Locate and identify every blood parasite.
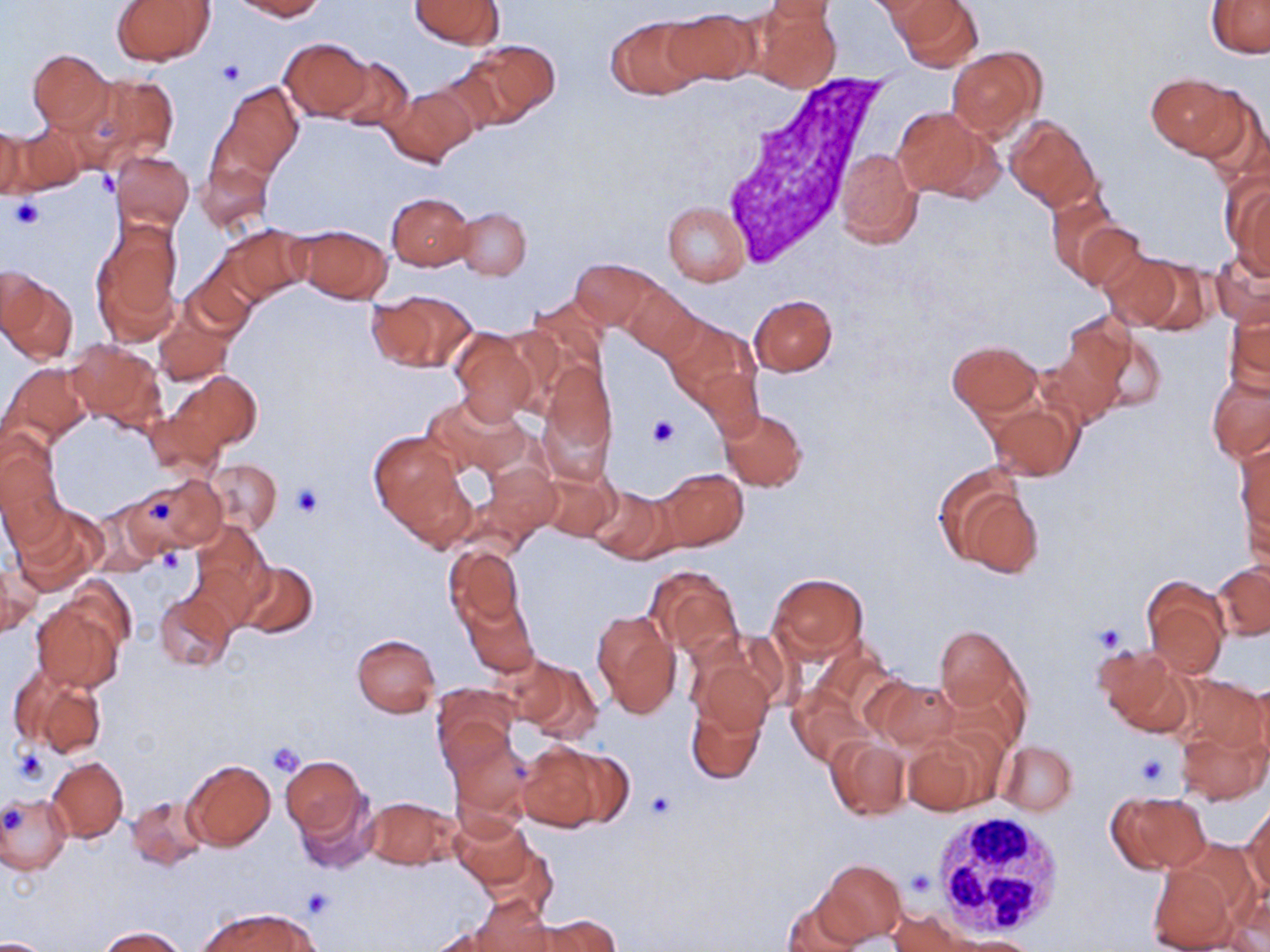

No blood parasites observed.

Approximate bounding boxes as (x1, y1, x2, y2) in pixels. White blood cell locations: (709, 71, 891, 265), (929, 811, 1064, 937). Platelet locations: (217, 61, 245, 87), (97, 170, 121, 197), (8, 198, 46, 230), (647, 416, 679, 447), (290, 485, 322, 519), (150, 499, 172, 519), (159, 550, 182, 573), (1092, 622, 1128, 653), (266, 742, 306, 778), (12, 746, 51, 784), (1134, 752, 1172, 790), (645, 791, 678, 823), (2, 808, 25, 835), (906, 870, 933, 897), (301, 887, 334, 918). Uninfected red blood cell locations: (234, 0, 325, 19), (410, 0, 502, 49), (764, 0, 840, 23), (896, 0, 980, 71), (113, 1, 216, 66), (1207, 2, 1270, 57), (663, 8, 758, 86), (753, 8, 840, 92), (607, 16, 705, 100), (281, 37, 373, 119), (460, 38, 560, 127), (27, 48, 113, 132), (947, 48, 1044, 139), (330, 55, 415, 132), (71, 73, 179, 169), (1147, 74, 1244, 157), (218, 82, 303, 176), (385, 86, 475, 165), (892, 106, 1000, 201), (1006, 116, 1099, 210), (0, 124, 26, 203), (6, 125, 85, 195), (834, 148, 922, 247), (111, 150, 194, 232), (196, 159, 272, 233), (1222, 175, 1270, 276), (387, 192, 475, 271), (1048, 194, 1124, 282), (661, 201, 749, 286), (457, 208, 530, 279), (89, 217, 182, 341), (1075, 222, 1149, 296), (222, 224, 309, 305), (291, 224, 395, 304), (1209, 248, 1270, 324), (1102, 251, 1193, 331), (570, 258, 657, 327), (180, 269, 256, 339), (1, 273, 77, 363), (624, 285, 700, 359), (367, 290, 475, 372), (526, 295, 608, 378), (750, 295, 836, 376), (1224, 300, 1269, 395), (155, 314, 233, 385), (664, 316, 759, 415), (448, 325, 540, 425), (1081, 325, 1167, 416), (1039, 335, 1125, 424), (65, 337, 166, 430), (948, 341, 1039, 418), (540, 362, 616, 467), (2, 363, 90, 447), (170, 373, 262, 457), (1207, 373, 1270, 463), (423, 394, 531, 481), (986, 401, 1081, 481), (719, 409, 807, 491), (144, 410, 224, 479), (0, 433, 65, 540), (369, 433, 463, 531), (1235, 440, 1270, 539), (207, 458, 282, 533), (484, 463, 562, 535), (935, 465, 1044, 578), (656, 469, 747, 550), (538, 471, 619, 542), (136, 472, 224, 552), (587, 486, 672, 563), (86, 502, 166, 576), (9, 505, 103, 595), (189, 520, 272, 622), (443, 545, 527, 633), (2, 558, 37, 640), (235, 560, 318, 639), (1214, 563, 1269, 640), (645, 565, 742, 657), (767, 572, 870, 664), (1143, 578, 1230, 677), (154, 588, 236, 672), (463, 597, 538, 676), (31, 600, 126, 694), (592, 610, 681, 719), (935, 625, 1019, 711), (351, 633, 441, 717), (1092, 645, 1188, 734), (492, 652, 572, 724), (692, 655, 776, 737), (521, 661, 602, 743), (13, 665, 108, 758), (1178, 672, 1268, 761), (1251, 678, 1270, 767), (871, 679, 961, 752), (433, 683, 520, 759), (787, 688, 870, 768), (685, 699, 766, 786), (1175, 725, 1267, 804), (446, 729, 530, 823), (900, 730, 994, 816), (827, 736, 909, 820), (997, 740, 1077, 816), (515, 742, 613, 832), (280, 754, 368, 843), (47, 757, 129, 842), (183, 758, 275, 851), (292, 786, 378, 874), (1109, 791, 1211, 873), (0, 792, 72, 873), (126, 794, 210, 871), (362, 795, 461, 869), (1244, 802, 1270, 899), (452, 815, 534, 888), (820, 859, 906, 943), (1146, 864, 1237, 952), (778, 891, 868, 952), (469, 897, 557, 951), (200, 909, 317, 952), (885, 909, 976, 951), (537, 914, 621, 952), (96, 927, 186, 951), (948, 934, 1042, 951), (0, 936, 53, 952). Slide-level diagnosis: negative for blood parasites. Light microscopy. Image is 1270×952 pixels. Single field of view. Captured at 1000x magnification. May-Grünwald-Giemsa stain. Thin blood smear.